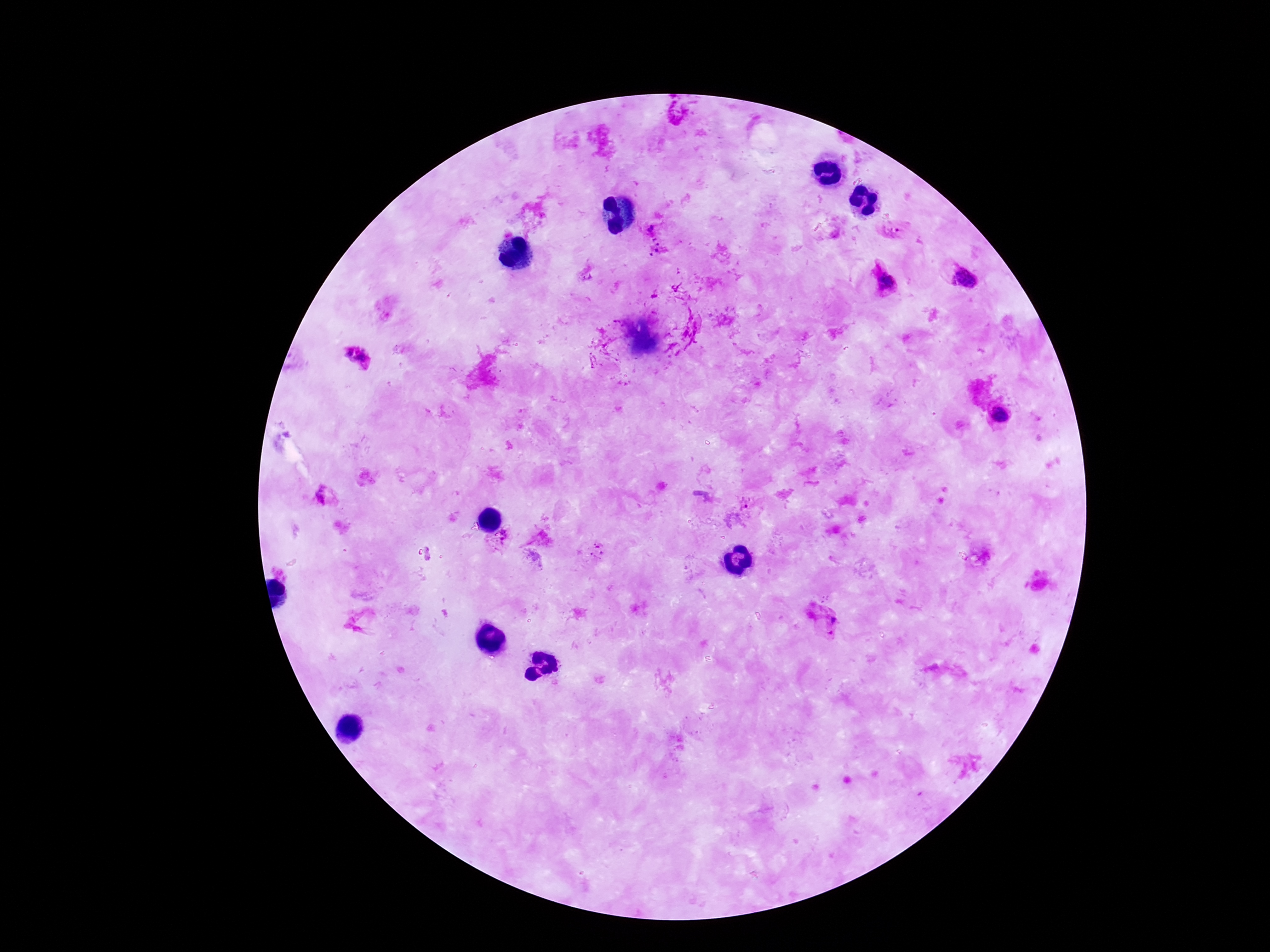

Approximate centers as {x, y} in pixels. Plasmodium parasite locations: {679, 114}, {650, 229}, {892, 230}, {656, 246}, {964, 278}, {887, 281}, {347, 354}, {363, 359}, {1000, 415}, {322, 497}, {748, 505}, {504, 536}, {597, 551}, {824, 617}. 100x magnification. Image is 1270×952 pixels. Giemsa-stained preparation. Photographed through the microscope eyepiece with a smartphone camera. Thick peripheral-blood smear. Patient malaria status: positive. One field from this slide.